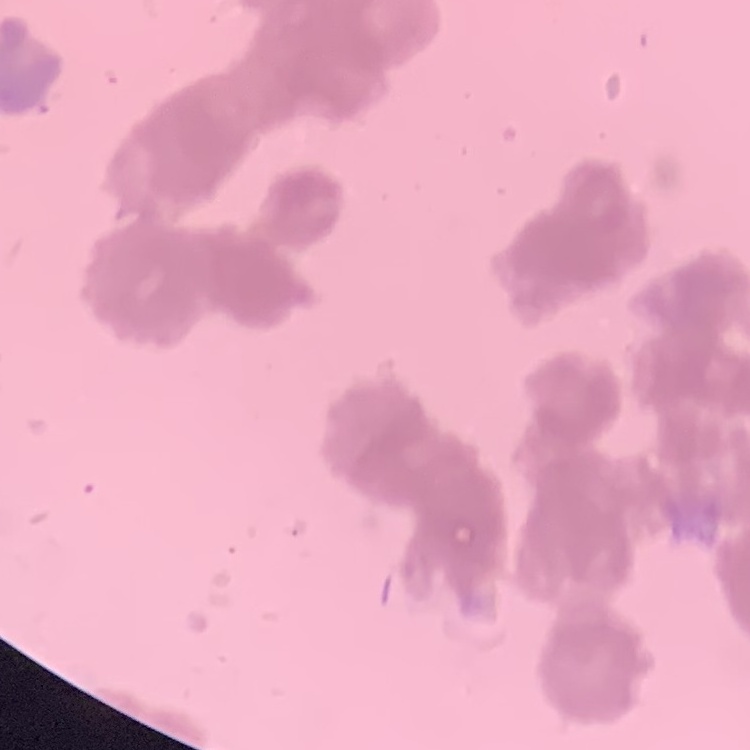

erythrocyte morphology = rouleaux formation
stain = Field's or Giemsa
image type = square crop of a larger photomicrograph
preparation = thin blood smear